Outline each blood parasite and name the species.
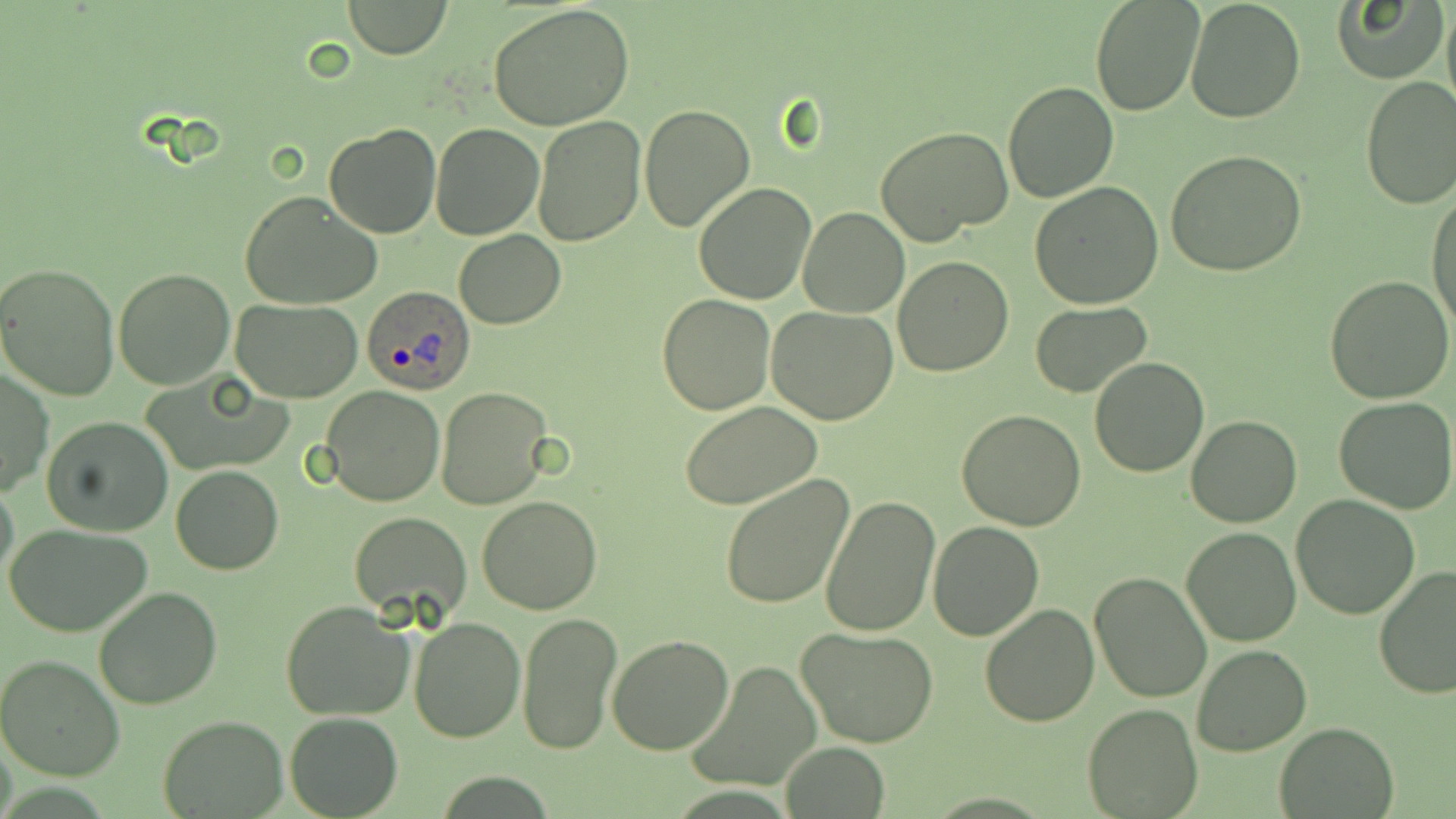
Approximate bounding boxes as (x1,y1)-(x2,y2) corner pairs in pixels.
Plasmodium ovale-infected red blood cells: (358,284)-(477,398).
No Plasmodium falciparum, Plasmodium malariae, Plasmodium vivax, Babesia divergens, or Trypanosoma brucei observed.

Uninfected red blood cell locations: (343,0)-(451,58), (1090,0)-(1205,118), (1185,0)-(1306,121), (1442,1)-(1456,121), (1334,2)-(1445,84), (487,3)-(635,130), (1358,75)-(1456,209), (1004,82)-(1117,202), (638,104)-(755,231), (531,116)-(646,246), (430,122)-(544,239), (323,124)-(443,239), (875,126)-(1013,247), (1166,151)-(1308,279), (693,181)-(816,303), (1030,182)-(1164,308), (1428,186)-(1456,332), (239,191)-(383,310), (797,208)-(908,318), (453,230)-(565,330), (893,255)-(1014,374), (0,262)-(119,403), (113,267)-(236,388), (1324,275)-(1456,406), (656,294)-(775,415), (232,298)-(365,402), (1029,302)-(1154,398), (765,308)-(897,426), (1089,356)-(1212,477), (2,368)-(52,497), (320,385)-(445,507), (436,387)-(552,509), (1333,395)-(1456,516), (680,400)-(823,510), (957,409)-(1087,530), (1186,415)-(1301,528), (40,416)-(173,537), (171,466)-(283,575), (0,473)-(20,599), (719,474)-(855,610), (1290,494)-(1422,621), (476,495)-(603,615), (821,495)-(941,635), (349,511)-(470,620), (927,520)-(1044,641), (8,524)-(154,637), (1180,526)-(1303,647), (1372,565)-(1456,701), (1089,571)-(1215,703), (93,587)-(223,710), (280,602)-(415,721), (979,603)-(1099,727), (517,611)-(622,756), (409,614)-(526,740), (794,627)-(940,750), (607,635)-(734,755), (1191,644)-(1311,756), (0,653)-(127,780), (687,661)-(823,794), (1083,703)-(1201,818), (285,711)-(402,818), (158,714)-(288,817), (1273,720)-(1400,819), (779,742)-(890,818). Slide-level diagnosis: Plasmodium ovale. Thin blood smear. Image is 1456×819 pixels. One field of a larger specimen. May-Grünwald-Giemsa stain. 1000x magnification. Optical microscopy.